State the blood parasite species.
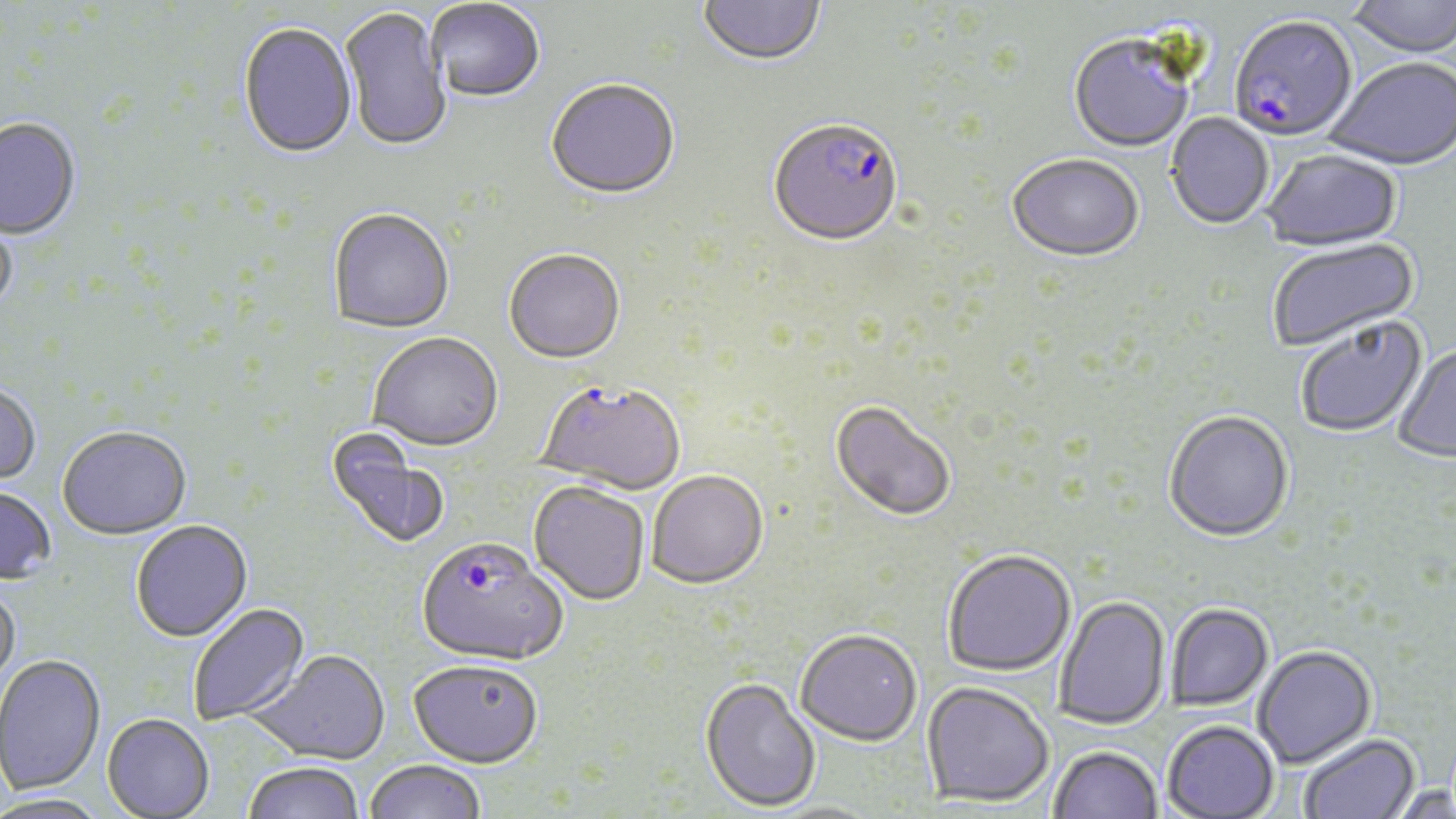

Plasmodium falciparum.

Approximate bounding boxes as [x1, y1, x2, y2] in pixels. Plasmodium falciparum-infected red blood cell locations: [1229, 18, 1358, 144], [768, 121, 903, 250], [536, 380, 685, 493], [416, 537, 568, 666]. Uninfected red blood cell locations: [698, 0, 826, 69], [1346, 0, 1456, 60], [427, 1, 545, 105], [340, 7, 451, 154], [238, 24, 357, 161], [1068, 37, 1194, 155], [1325, 60, 1455, 172], [546, 81, 680, 202], [1166, 114, 1273, 231], [0, 120, 81, 241], [1262, 150, 1402, 253], [1008, 156, 1144, 264], [0, 203, 17, 319], [328, 210, 454, 335], [1267, 238, 1420, 355], [504, 251, 625, 366], [1294, 316, 1429, 439], [368, 334, 504, 454], [1392, 344, 1456, 465], [0, 383, 41, 486], [831, 400, 956, 521], [1163, 412, 1294, 543], [57, 428, 191, 541], [324, 428, 451, 552], [647, 470, 768, 587], [528, 481, 650, 605], [0, 486, 57, 585], [131, 521, 253, 643], [942, 549, 1076, 677], [0, 582, 21, 697], [1054, 596, 1171, 730], [188, 603, 311, 726], [1166, 603, 1274, 710], [795, 628, 923, 745], [1253, 646, 1377, 769], [248, 650, 391, 766], [1, 656, 105, 797], [408, 659, 544, 767], [700, 677, 822, 812], [922, 682, 1054, 808], [101, 714, 214, 818], [1161, 720, 1279, 818], [1299, 734, 1420, 819], [1048, 746, 1162, 819], [363, 759, 486, 819], [243, 762, 365, 819], [1386, 784, 1455, 818], [0, 795, 111, 819]. Optical microscopy. Single field of view. Image is 1456×819 pixels. 1000x magnification. Thin blood film. May-Grünwald-Giemsa stain.